Locate malaria parasites and leukocytes.
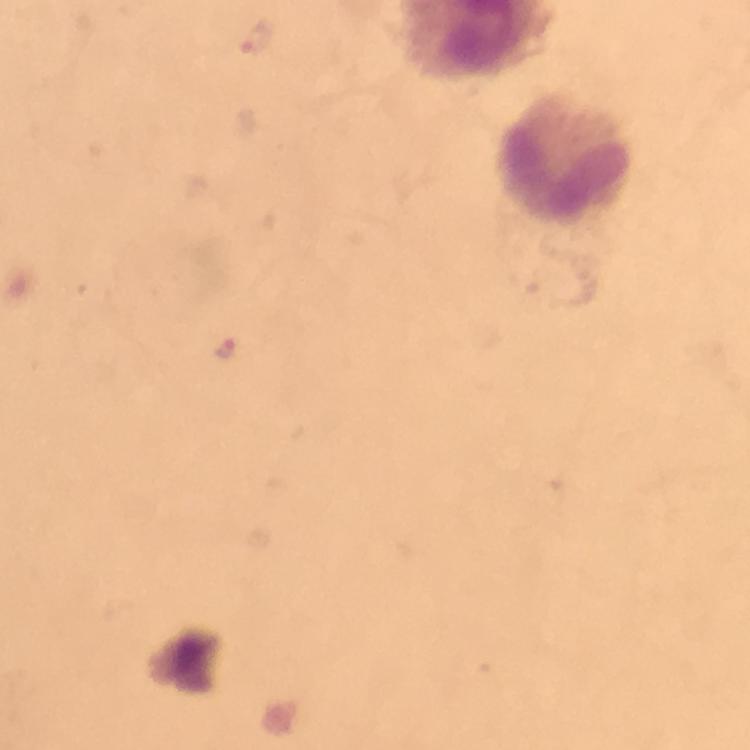
Approximate centers as [x, y] in pixels.
Malaria parasites: [257, 37], [224, 349].
Leukocytes: [566, 160].

Image is 750×750 pixels. Thick blood film. At 100x magnification. Smartphone photograph taken through a microscope. Giemsa stain. Immersion oil was used. From a diagnostic examination for malaria. Cropped region of a single field of view.